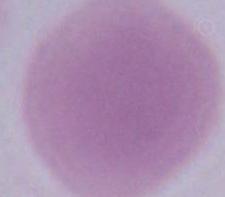

Photomicrograph. An erythrocyte is seen. 1000x magnification.